Report the malaria status of this cell.
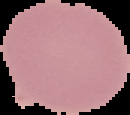

Uninfected.

image size = 130×115 pixels
image type = segmented cell region with the area outside set to black
preparation = thin blood smear